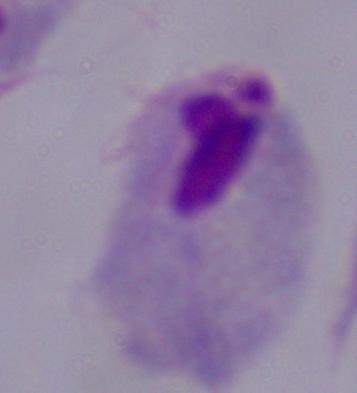
{
  "identification": "trichomonad",
  "modality": "photomicrograph",
  "magnification": "1000x"
}